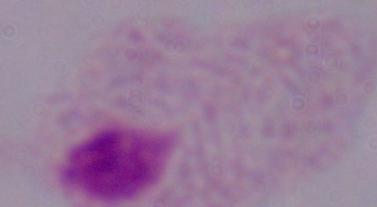

magnification = 1000x
identification = trichomonad
modality = micrograph